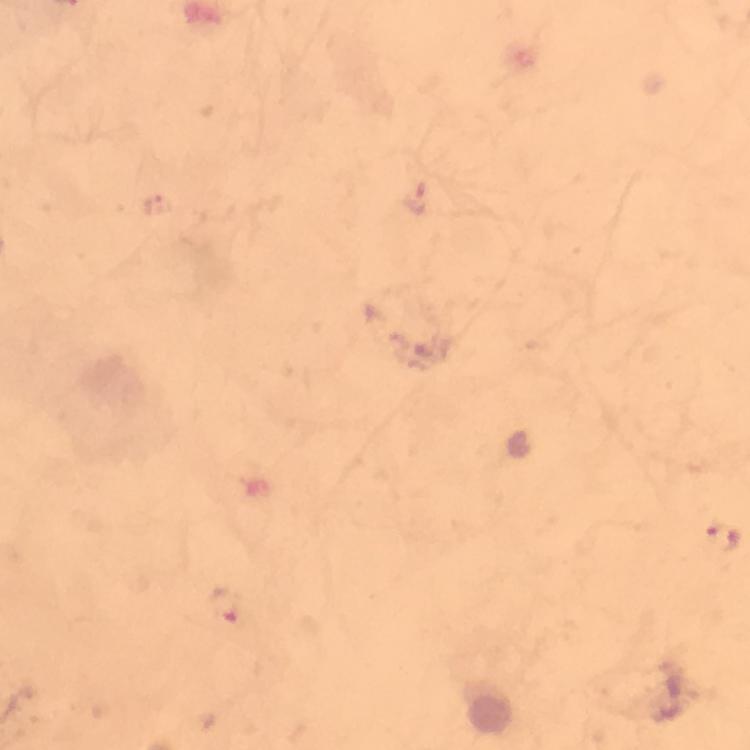 Approximate centers as [x, y] in pixels. Plasmodium parasite locations: [723, 538], [223, 607]. Image is 750×750 pixels. Cropped region of a single field of view. Giemsa-stained preparation. At 100x magnification. Photographed through the microscope with a smartphone camera. Thick blood film. From a diagnostic examination for malaria. Immersion oil applied.